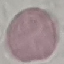 Result: negative for malaria parasites. Photographed with a smartphone camera at the microscope eyepiece. Thin blood film. Cell patch, automatically extracted from a larger field of view and resized to 64 × 64 pixels. Giemsa stain.